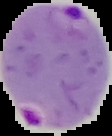 Malaria status: parasitized. Segmented cell region on a black background. Image is 112×136 pixels. From a thin blood film.